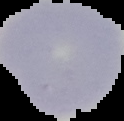 Malaria status: uninfected. Segmented cell region on a black background. Image is 124×121 pixels. From a thin blood film.